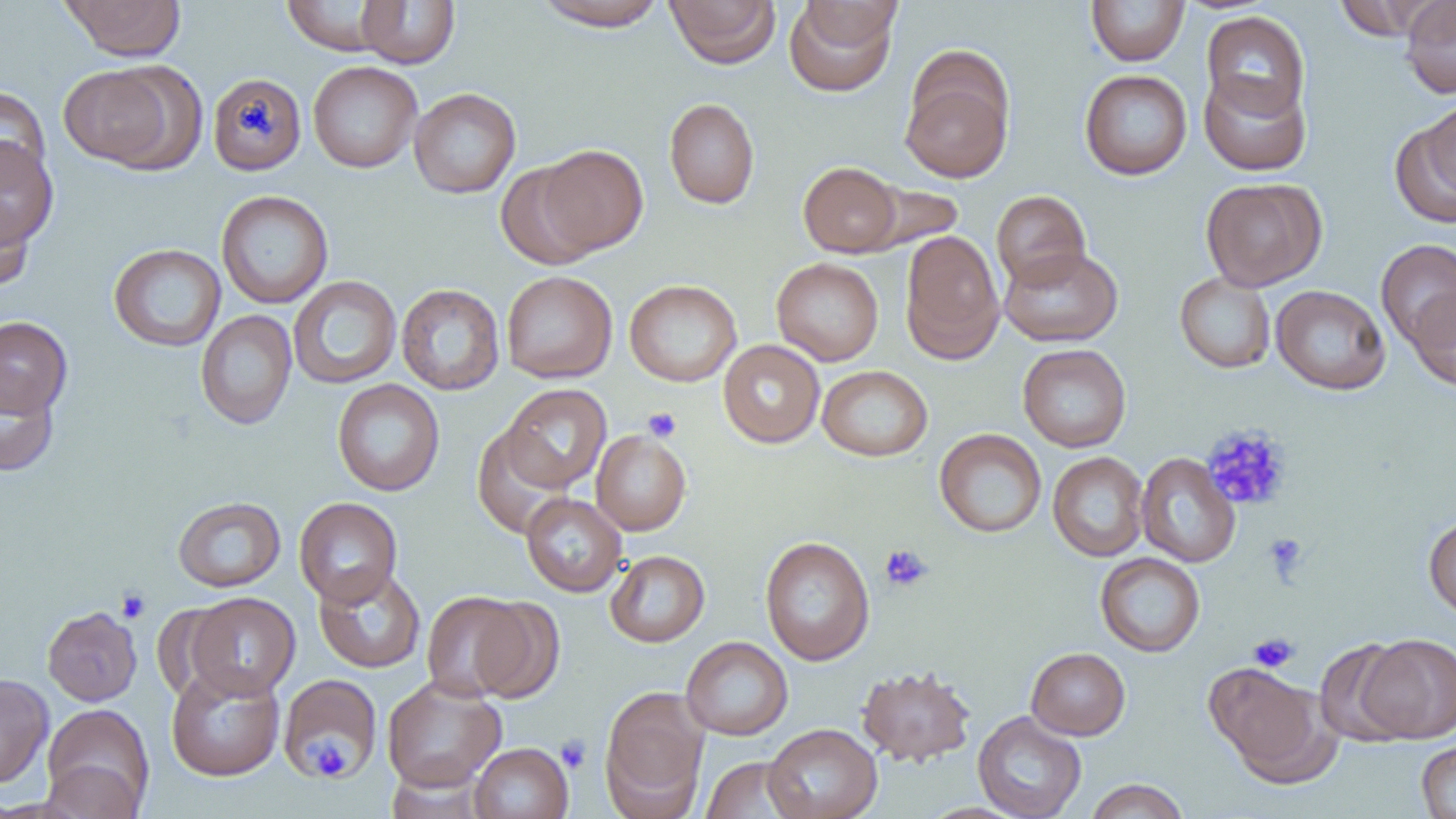
Approximate bounding boxes as (x1, y1, x2, y2) in pixels. Uninfected red blood cell locations: (60, 0, 186, 61), (355, 0, 460, 68), (532, 0, 669, 31), (665, 0, 781, 68), (784, 0, 900, 97), (1332, 0, 1439, 41), (1399, 0, 1456, 98), (281, 1, 392, 55), (1086, 1, 1190, 66), (1201, 11, 1310, 121), (308, 61, 422, 173), (900, 61, 1016, 184), (58, 63, 186, 171), (1079, 70, 1193, 180), (1198, 70, 1312, 176), (208, 72, 307, 175), (0, 86, 50, 187), (409, 88, 521, 198), (1423, 97, 1456, 196), (664, 98, 760, 208), (1390, 116, 1456, 229), (0, 137, 59, 248), (537, 144, 648, 255), (495, 160, 602, 271), (798, 161, 903, 257), (1200, 177, 1326, 291), (857, 182, 965, 254), (216, 190, 333, 309), (991, 190, 1091, 290), (0, 195, 35, 292), (899, 230, 1005, 363), (1376, 239, 1456, 349), (108, 243, 226, 352), (999, 245, 1123, 347), (771, 257, 884, 365), (501, 270, 617, 383), (1174, 272, 1276, 373), (288, 275, 402, 389), (624, 279, 742, 386), (396, 283, 505, 396), (1270, 284, 1391, 395), (1408, 286, 1456, 391), (195, 309, 297, 430), (0, 316, 73, 418), (718, 340, 825, 448), (1017, 343, 1131, 452), (817, 365, 933, 462), (0, 366, 60, 477), (332, 379, 445, 496), (501, 383, 612, 492), (472, 426, 575, 539), (934, 428, 1047, 538), (591, 430, 691, 535), (1047, 451, 1149, 562), (1135, 453, 1241, 568), (521, 493, 627, 597), (172, 496, 286, 592), (294, 497, 403, 607), (1423, 514, 1456, 619), (760, 535, 875, 666), (605, 550, 709, 647), (1095, 552, 1206, 657), (313, 565, 426, 673), (421, 591, 529, 701), (185, 592, 300, 700), (468, 596, 564, 704), (42, 606, 142, 706), (1357, 633, 1456, 743), (681, 636, 793, 740), (1314, 638, 1416, 746), (1026, 647, 1131, 740), (1204, 661, 1339, 785), (166, 663, 285, 781), (857, 664, 977, 767), (277, 672, 384, 781), (0, 673, 53, 789), (381, 676, 506, 792), (599, 687, 709, 815), (42, 703, 155, 816), (973, 711, 1087, 819), (764, 723, 882, 819), (1417, 740, 1456, 818), (469, 742, 573, 819), (700, 756, 807, 818), (40, 759, 146, 819), (1084, 778, 1190, 819), (917, 802, 1031, 819). Platelet locations: (643, 408, 681, 442), (1201, 424, 1293, 511), (1264, 533, 1308, 581), (880, 544, 933, 592), (116, 588, 151, 623), (1248, 632, 1299, 672), (556, 735, 591, 774), (309, 736, 349, 781). Slide-level diagnosis: negative for blood parasites. Light microscopy. Image is 1456×819 pixels. Captured at 1000x magnification. Thin blood smear. One field of a larger specimen.